Assess the morphology of the erythrocytes.
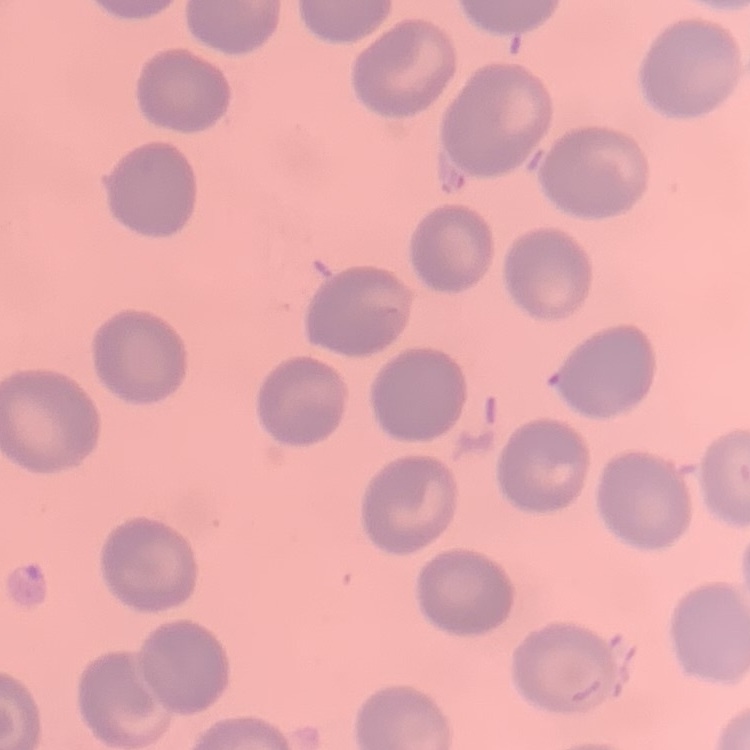

No rouleaux formation.

Summary:
  - Stain: Field's or Giemsa
  - Preparation: thin blood film
  - Image type: one tile cut from a larger photomicrograph